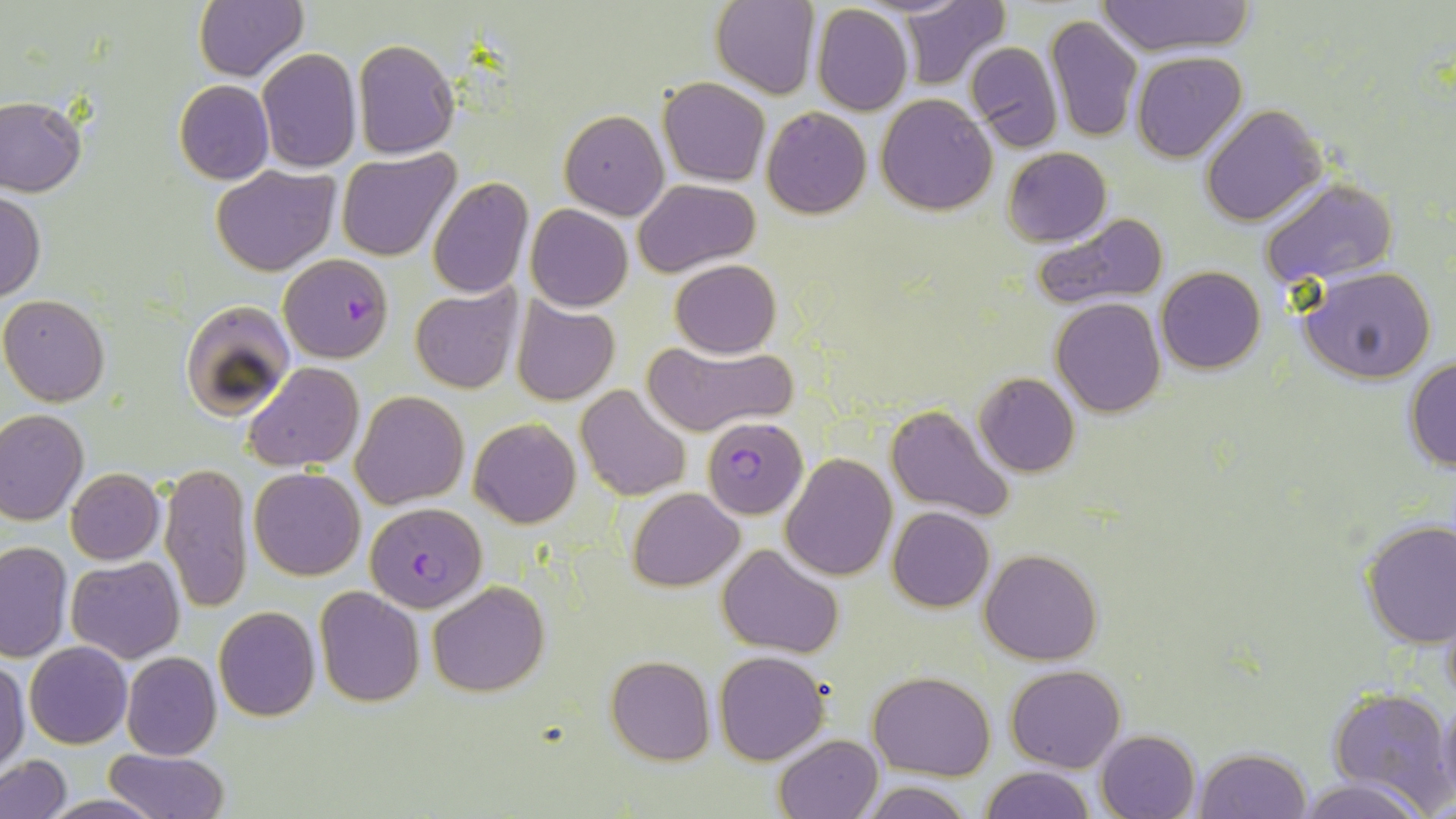

Approximate bounding boxes as [x1, y1, x2, y2] in pixels. Plasmodium falciparum-infected red blood cell locations: [278, 253, 395, 363], [701, 417, 808, 519], [365, 501, 487, 612]. Uninfected red blood cell locations: [192, 0, 308, 83], [711, 0, 818, 100], [898, 0, 1012, 90], [1096, 1, 1254, 55], [811, 5, 912, 116], [1044, 14, 1143, 144], [351, 38, 460, 160], [965, 41, 1064, 152], [256, 48, 363, 174], [1131, 51, 1246, 161], [659, 77, 770, 187], [173, 80, 273, 184], [877, 93, 998, 215], [0, 97, 87, 196], [1200, 104, 1326, 226], [762, 107, 871, 219], [559, 110, 669, 221], [1002, 146, 1112, 247], [335, 149, 460, 262], [212, 166, 340, 276], [428, 177, 533, 298], [632, 179, 760, 276], [1260, 179, 1397, 289], [0, 189, 44, 304], [526, 205, 632, 311], [1030, 210, 1173, 313], [670, 259, 780, 359], [1156, 266, 1265, 374], [1300, 268, 1437, 384], [411, 281, 522, 396], [1, 294, 111, 407], [510, 296, 621, 406], [1051, 298, 1167, 417], [181, 299, 296, 417], [643, 340, 796, 436], [1403, 357, 1456, 472], [243, 361, 362, 472], [973, 373, 1080, 477], [575, 385, 690, 501], [352, 391, 468, 510], [887, 404, 1017, 523], [0, 409, 89, 526], [469, 418, 580, 528], [781, 453, 897, 581], [159, 463, 254, 613], [249, 466, 366, 580], [65, 467, 165, 564], [629, 488, 743, 590], [888, 506, 994, 612], [1358, 518, 1456, 647], [1, 541, 73, 663], [718, 543, 844, 657], [980, 548, 1102, 664], [67, 556, 185, 664], [427, 580, 549, 696], [314, 586, 424, 708], [1440, 591, 1456, 715], [212, 606, 320, 723], [25, 641, 133, 749], [714, 650, 828, 764], [121, 651, 222, 761], [605, 655, 714, 765], [0, 657, 29, 772], [1006, 665, 1125, 773], [869, 672, 994, 779], [1327, 688, 1453, 812], [1435, 692, 1456, 807], [1095, 728, 1200, 818], [774, 734, 884, 819], [1193, 747, 1311, 819], [105, 748, 229, 819], [1, 755, 71, 818], [979, 765, 1094, 819], [1292, 777, 1434, 819], [858, 780, 978, 818], [38, 795, 167, 818]. Slide-level diagnosis: Plasmodium falciparum. Thin blood film. Image is 1456×819 pixels. Captured at 1000x magnification. Single field of view. May-Grünwald-Giemsa stain. Optical microscopy.